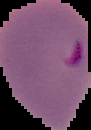
Summary:
  - Image size: 91×130 pixels
  - Image type: segmented cell region with the area outside set to black
  - Preparation: thin blood smear
  - Malaria status: parasitized